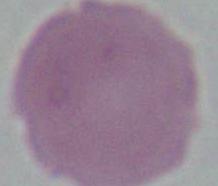
Summary:
  - Identification: erythrocyte
  - Magnification: 1000x
  - Modality: photomicrograph